Point out each malaria parasite.
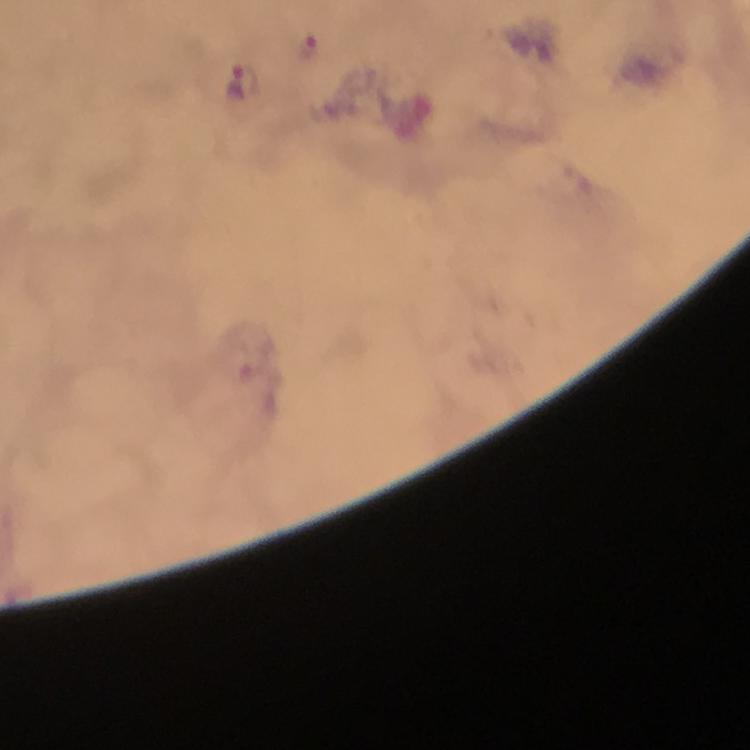

Approximate centers as (x, y) in pixels.
Malaria parasites: (309, 49), (244, 81).

Summary:
  - Context: from a diagnostic examination for malaria
  - Magnification: 100x
  - Image size: 750×750 pixels
  - Capture: smartphone mounted on the microscope
  - Immersion oil: applied
  - Stain: Giemsa
  - Cropped from: a single field of view
  - Preparation: thick smear